Assess this cell for malaria.
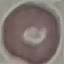

It is uninfected.

capture = smartphone camera at the microscope eyepiece
stain = Giemsa
preparation = thin blood film
image type = cell patch, automatically extracted from a larger field of view and resized to 64 × 64 pixels